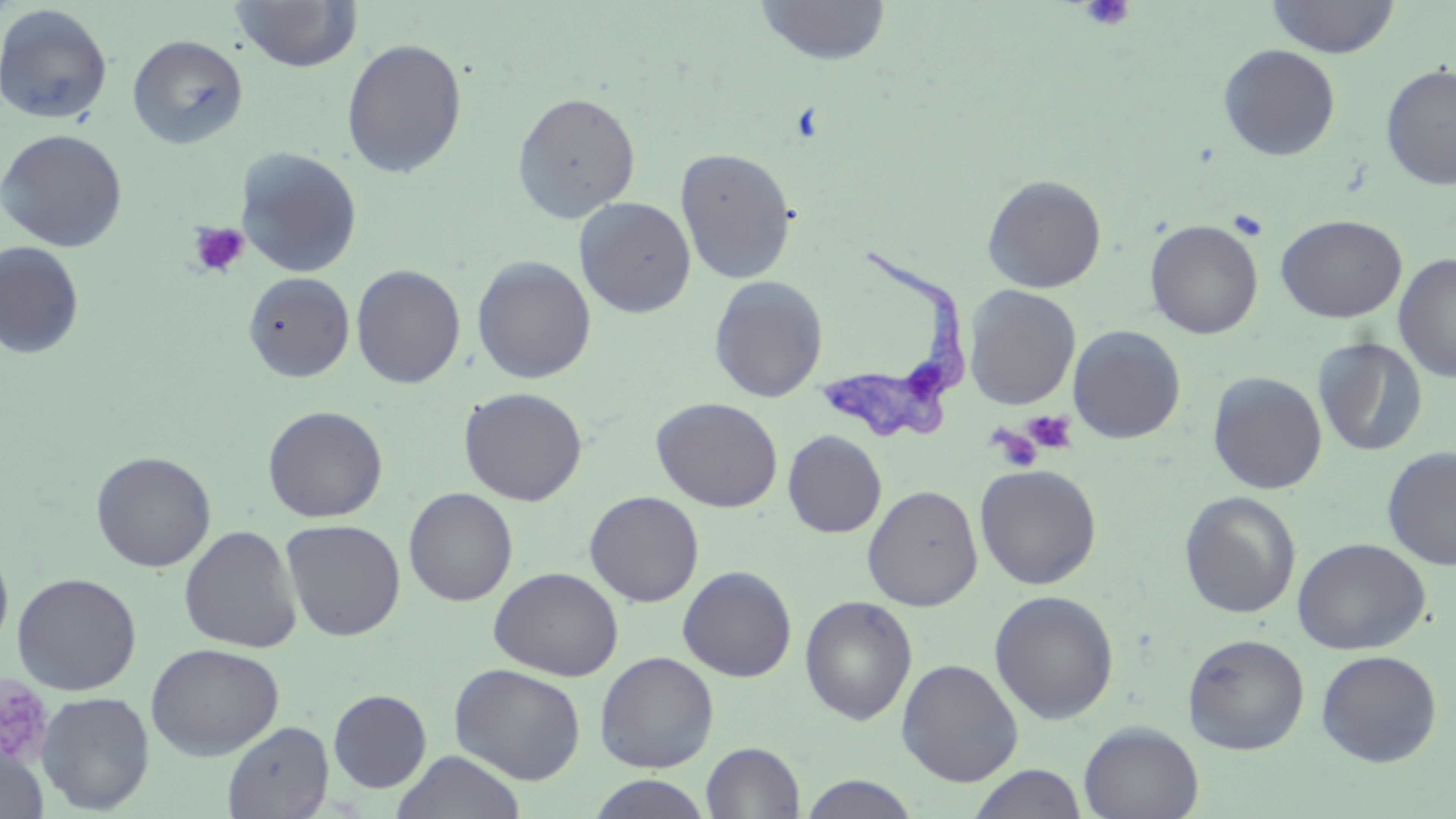

Summary:
  - Coordinate format: approximate bounding boxes as named x1/y1/x2/y2 corners in pixels
  - Platelet locations: (x1=1079, y1=0, x2=1136, y2=33), (x1=1226, y1=208, x2=1270, y2=241), (x1=187, y1=222, x2=250, y2=279), (x1=1024, y1=410, x2=1077, y2=453), (x1=997, y1=415, x2=1071, y2=465), (x1=989, y1=425, x2=1043, y2=471), (x1=0, y1=678, x2=53, y2=764)
  - Uninfected red blood cell locations: (x1=230, y1=0, x2=363, y2=73), (x1=754, y1=0, x2=892, y2=64), (x1=1265, y1=0, x2=1400, y2=58), (x1=0, y1=4, x2=114, y2=125), (x1=127, y1=34, x2=249, y2=150), (x1=341, y1=38, x2=467, y2=178), (x1=1218, y1=44, x2=1341, y2=161), (x1=1379, y1=63, x2=1456, y2=190), (x1=512, y1=91, x2=641, y2=222), (x1=0, y1=129, x2=128, y2=252), (x1=235, y1=147, x2=363, y2=278), (x1=675, y1=147, x2=797, y2=285), (x1=982, y1=174, x2=1107, y2=293), (x1=574, y1=196, x2=696, y2=318), (x1=1275, y1=214, x2=1407, y2=323), (x1=1145, y1=219, x2=1264, y2=339), (x1=0, y1=242, x2=85, y2=360), (x1=1394, y1=253, x2=1456, y2=381), (x1=472, y1=255, x2=596, y2=384), (x1=350, y1=264, x2=466, y2=389), (x1=242, y1=271, x2=355, y2=382), (x1=708, y1=275, x2=828, y2=403), (x1=964, y1=285, x2=1081, y2=410), (x1=1067, y1=325, x2=1186, y2=444), (x1=1313, y1=336, x2=1428, y2=457), (x1=1208, y1=372, x2=1327, y2=494), (x1=459, y1=387, x2=588, y2=506), (x1=651, y1=397, x2=783, y2=512), (x1=262, y1=404, x2=387, y2=523), (x1=783, y1=430, x2=886, y2=538), (x1=1381, y1=447, x2=1456, y2=570), (x1=91, y1=451, x2=216, y2=572), (x1=974, y1=464, x2=1101, y2=590), (x1=863, y1=485, x2=983, y2=611), (x1=403, y1=487, x2=518, y2=606), (x1=584, y1=491, x2=704, y2=607), (x1=1179, y1=491, x2=1301, y2=618), (x1=280, y1=518, x2=406, y2=641), (x1=179, y1=524, x2=302, y2=653), (x1=1293, y1=537, x2=1430, y2=655), (x1=0, y1=543, x2=14, y2=656), (x1=678, y1=565, x2=797, y2=682), (x1=489, y1=566, x2=624, y2=681), (x1=12, y1=572, x2=142, y2=695), (x1=989, y1=590, x2=1119, y2=724), (x1=800, y1=595, x2=918, y2=725), (x1=1183, y1=632, x2=1310, y2=754), (x1=146, y1=643, x2=284, y2=759), (x1=1316, y1=649, x2=1442, y2=767), (x1=594, y1=651, x2=720, y2=772), (x1=896, y1=658, x2=1023, y2=786), (x1=449, y1=663, x2=587, y2=785), (x1=327, y1=689, x2=432, y2=793), (x1=36, y1=691, x2=155, y2=813), (x1=223, y1=720, x2=333, y2=819), (x1=1077, y1=720, x2=1204, y2=819), (x1=702, y1=742, x2=805, y2=819), (x1=0, y1=744, x2=49, y2=819), (x1=391, y1=750, x2=526, y2=819), (x1=967, y1=763, x2=1089, y2=819), (x1=586, y1=774, x2=713, y2=818), (x1=798, y1=775, x2=922, y2=818)
  - Trypanosoma brucei locations: (x1=814, y1=244, x2=982, y2=447)
  - Slide-level diagnosis: Trypanosoma brucei
  - Magnification: 1000x
  - Preparation: thin blood smear
  - Image size: 1456×819 pixels
  - Stain: May-Grünwald-Giemsa
  - Field of view: one of a larger specimen
  - Modality: optical microscopy